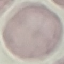
malaria status = uninfected
preparation = thin smear
stain = Giemsa
image type = automatically extracted cell patch, resized to 64 × 64 pixels
capture = smartphone through the microscope eyepiece